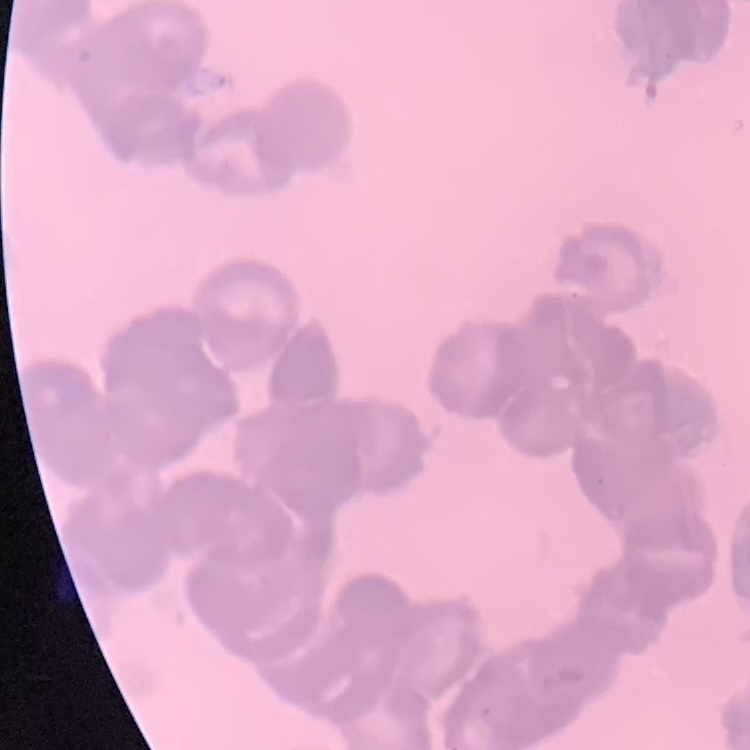 The erythrocytes show rouleaux formation. Field's or Giemsa stain. Square crop of a larger photomicrograph. Thin blood smear.